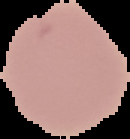

{
  "result": "negative for Plasmodium parasites",
  "image_size": "130×139 pixels",
  "image_type": "segmented cell region on a black background",
  "preparation": "thin blood film"
}